Describe the morphology of the erythrocytes.
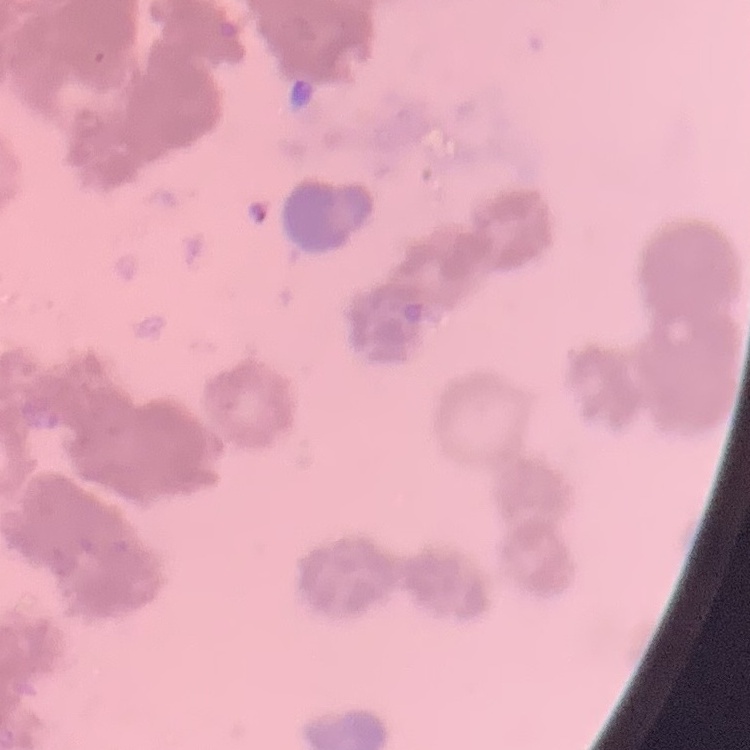
They show rouleaux formation.

Summary:
  - Preparation: thin blood smear
  - Image type: square crop of a larger photomicrograph
  - Stain: Field's or Giemsa